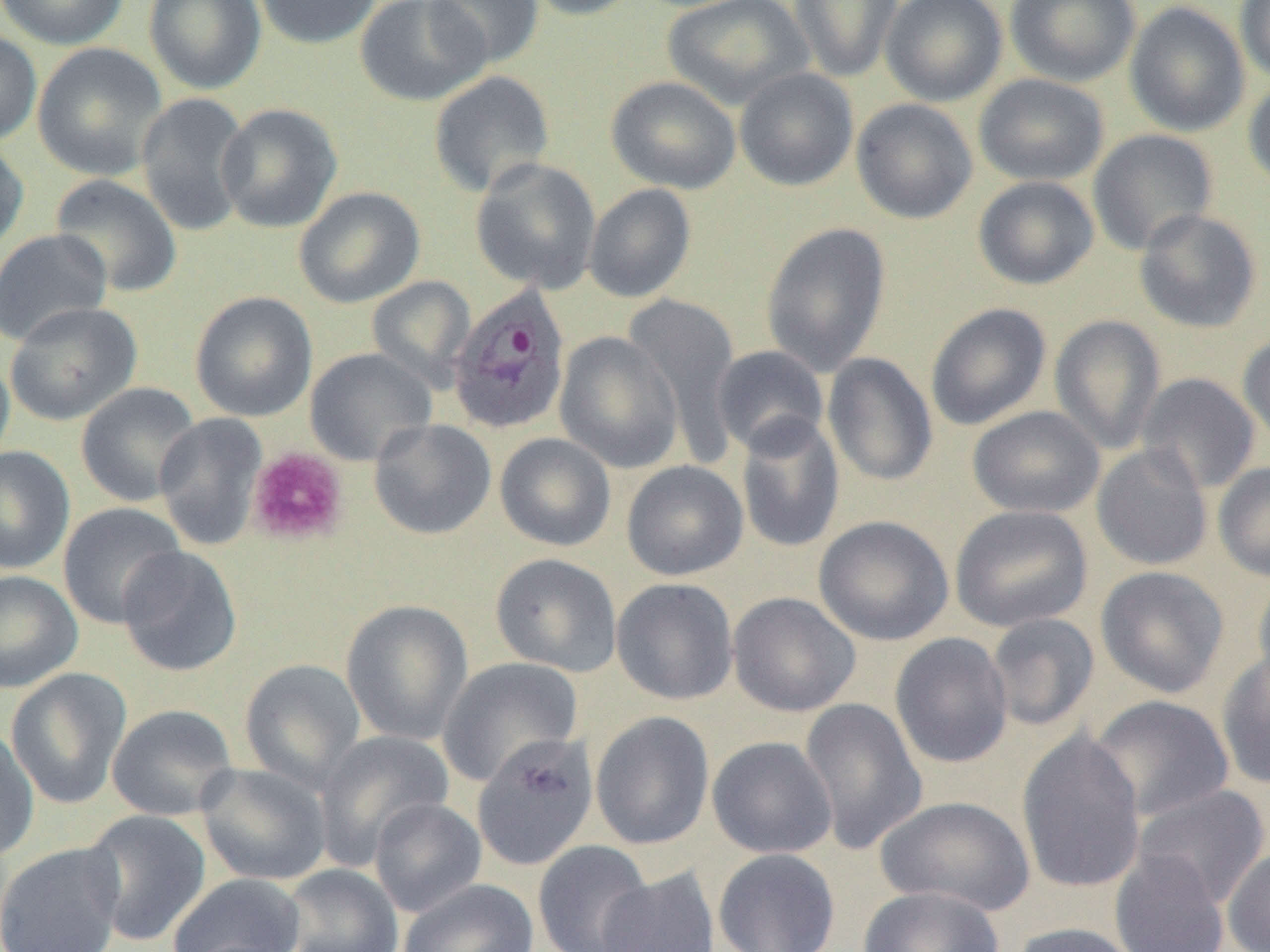
Approximate bounding boxes as (x1,y1)-(x2,y2) corner pairs in pixels. Plasmodium ovale-infected red blood cell locations: (448,285)-(572,434). Uninfected red blood cell locations: (0,0)-(130,50), (144,0)-(267,95), (253,0)-(383,49), (355,0)-(490,107), (424,0)-(544,69), (522,0)-(644,21), (661,0)-(813,110), (789,0)-(903,83), (880,0)-(1008,106), (1004,0)-(1141,87), (1234,0)-(1270,83), (1124,1)-(1250,137), (0,28)-(42,147), (33,43)-(168,180), (734,67)-(859,191), (428,70)-(555,197), (973,73)-(1110,186), (1243,74)-(1270,193), (605,75)-(741,194), (135,92)-(252,236), (851,98)-(978,224), (216,103)-(343,233), (1087,128)-(1219,255), (0,137)-(29,257), (469,157)-(602,294), (49,173)-(183,298), (972,175)-(1099,290), (584,183)-(696,302), (293,186)-(425,308), (1134,208)-(1262,333), (761,221)-(891,377), (0,229)-(113,347), (367,275)-(476,391), (190,291)-(318,422), (622,292)-(742,462), (4,300)-(142,426), (925,303)-(1052,430), (1049,314)-(1167,455), (554,331)-(683,473), (1238,332)-(1270,453), (711,345)-(829,457), (304,347)-(437,466), (0,348)-(15,473), (823,353)-(938,486), (1136,372)-(1261,494), (75,382)-(202,508), (967,405)-(1105,519), (153,413)-(268,551), (735,414)-(845,553), (368,418)-(497,540), (494,432)-(616,551), (1092,443)-(1213,571), (0,446)-(75,574), (621,460)-(748,581), (1213,462)-(1270,582), (58,502)-(186,629), (950,505)-(1094,632), (814,515)-(954,646), (117,546)-(242,677), (490,552)-(623,677), (1095,565)-(1230,698), (0,570)-(82,693), (1251,575)-(1270,704), (611,577)-(738,705), (727,592)-(861,717), (340,599)-(473,746), (985,612)-(1100,732), (889,632)-(1014,769), (1215,649)-(1270,790), (438,656)-(584,787), (239,658)-(366,791), (5,668)-(132,809), (1089,695)-(1235,821), (799,698)-(927,856), (106,704)-(239,821), (590,711)-(715,850), (0,722)-(39,862), (1016,728)-(1147,895), (313,730)-(454,869), (471,732)-(598,871), (707,736)-(837,858), (195,763)-(333,886), (1132,784)-(1270,909), (875,795)-(1036,916), (368,797)-(486,917), (81,809)-(211,946), (532,840)-(655,952), (0,842)-(125,952), (1222,845)-(1270,952), (712,848)-(841,952), (1109,850)-(1230,952), (280,864)-(404,952), (596,866)-(721,952), (168,873)-(306,952), (398,879)-(538,952), (858,885)-(1004,952), (1008,922)-(1143,952). Platelet locations: (246,447)-(348,545). Slide-level diagnosis: Plasmodium ovale. Image is 1270×952 pixels. Optical microscopy. One field of a larger specimen. Thin blood film. 1000x magnification.